Locate every Trypanosoma brucei.
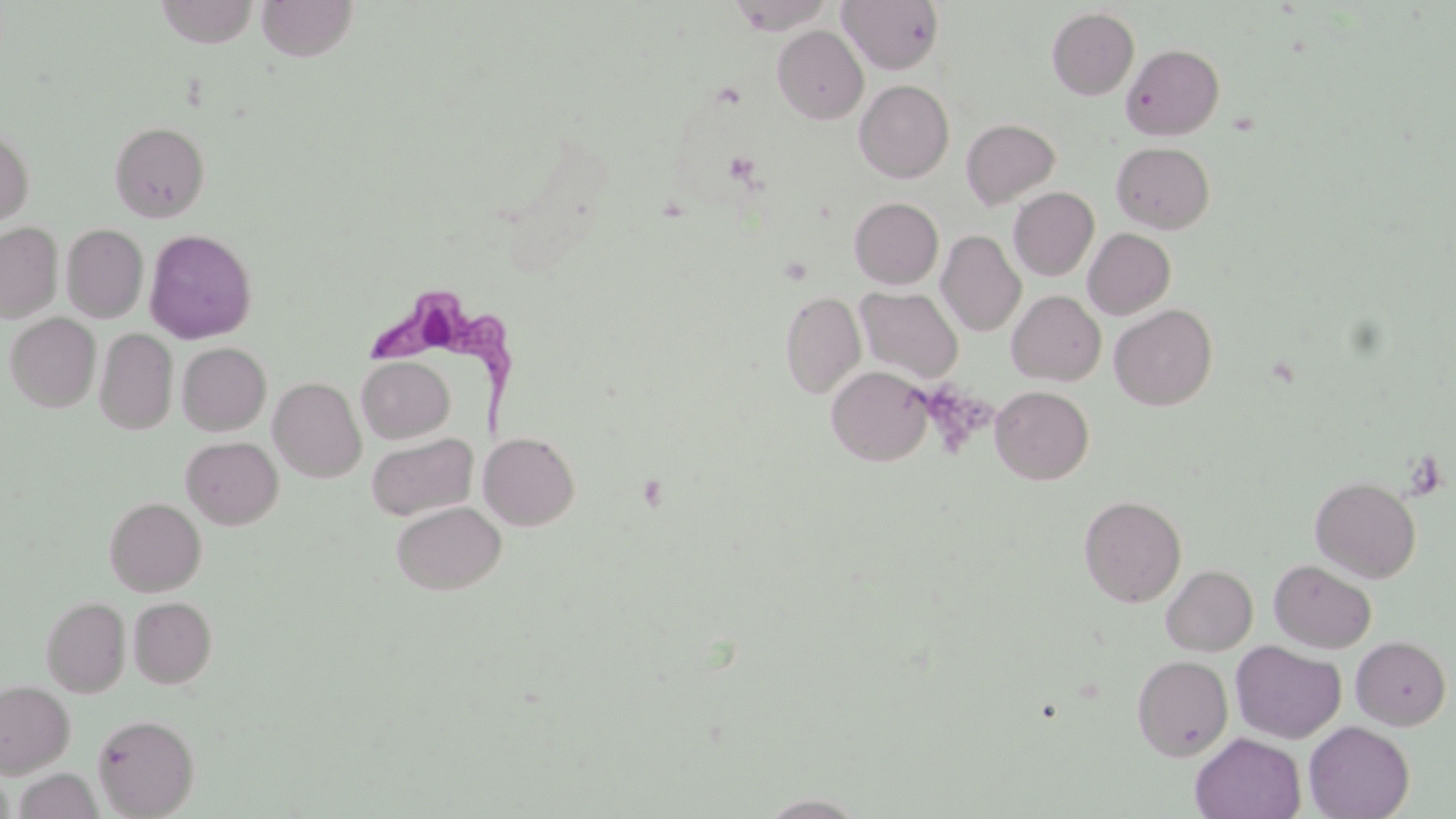
Approximate bounding boxes as [x1, y1, x2, y2] in pixels.
Trypanosoma brucei: [363, 289, 532, 427].

Summary:
  - Uninfected red blood cell locations: [155, 0, 259, 47], [256, 0, 359, 62], [727, 0, 835, 35], [838, 1, 946, 74], [1047, 8, 1139, 100], [773, 26, 868, 124], [1121, 44, 1224, 140], [854, 80, 954, 183], [961, 118, 1061, 209], [109, 121, 210, 223], [0, 127, 34, 228], [1111, 142, 1215, 233], [1008, 187, 1099, 281], [849, 197, 943, 289], [0, 223, 62, 322], [61, 224, 149, 323], [1083, 228, 1176, 319], [145, 229, 257, 344], [936, 230, 1026, 337], [856, 287, 964, 383], [1007, 291, 1106, 386], [780, 292, 866, 399], [1109, 304, 1217, 410], [5, 313, 100, 412], [95, 328, 177, 434], [177, 342, 271, 435], [357, 356, 454, 443], [826, 365, 933, 466], [269, 377, 366, 482], [990, 385, 1094, 484], [366, 432, 477, 521], [479, 432, 580, 531], [181, 436, 283, 529], [1310, 476, 1421, 583], [1078, 495, 1187, 607], [104, 497, 206, 596], [391, 501, 506, 595], [1268, 559, 1376, 653], [1161, 565, 1258, 655], [41, 596, 130, 697], [128, 596, 217, 688], [1351, 636, 1451, 730], [1231, 640, 1346, 743], [1132, 655, 1233, 760], [0, 680, 74, 777], [92, 713, 200, 818], [1304, 721, 1414, 819], [1190, 733, 1306, 819], [14, 768, 102, 819], [757, 792, 870, 818]
  - Platelet locations: [918, 381, 993, 457]
  - Slide-level diagnosis: Trypanosoma brucei
  - Magnification: 1000x
  - Modality: light microscopy
  - Stain: May-Grünwald-Giemsa
  - Image size: 1456×819 pixels
  - Preparation: thin blood film
  - Field of view: single